Assess the morphology of the red blood cells.
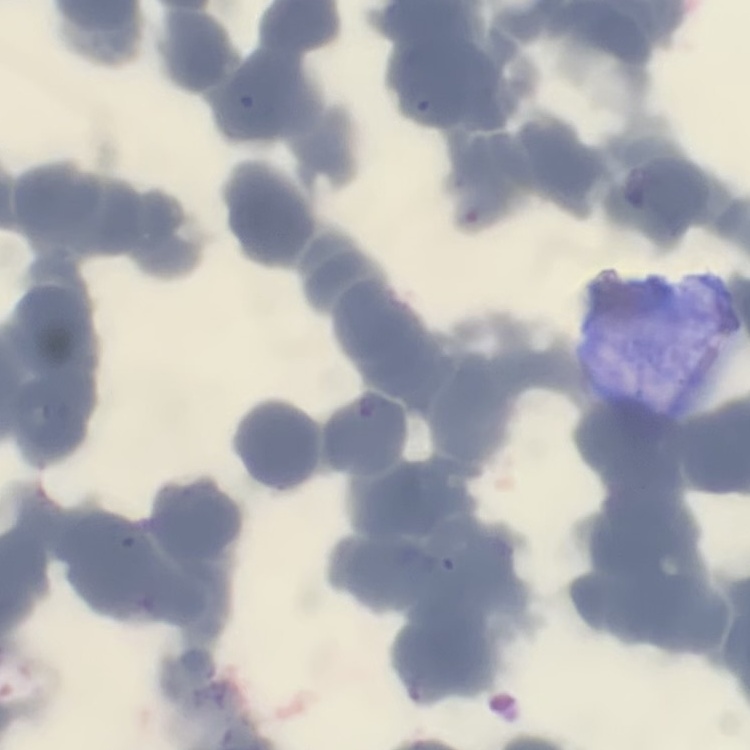
They show rouleaux formation.

image type = square crop of a larger photomicrograph
preparation = thin blood smear
stain = Field's or Giemsa